Identify the cell.
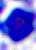

A leukocyte.

Summary:
  - Modality: photomicrograph
  - Magnification: 400x